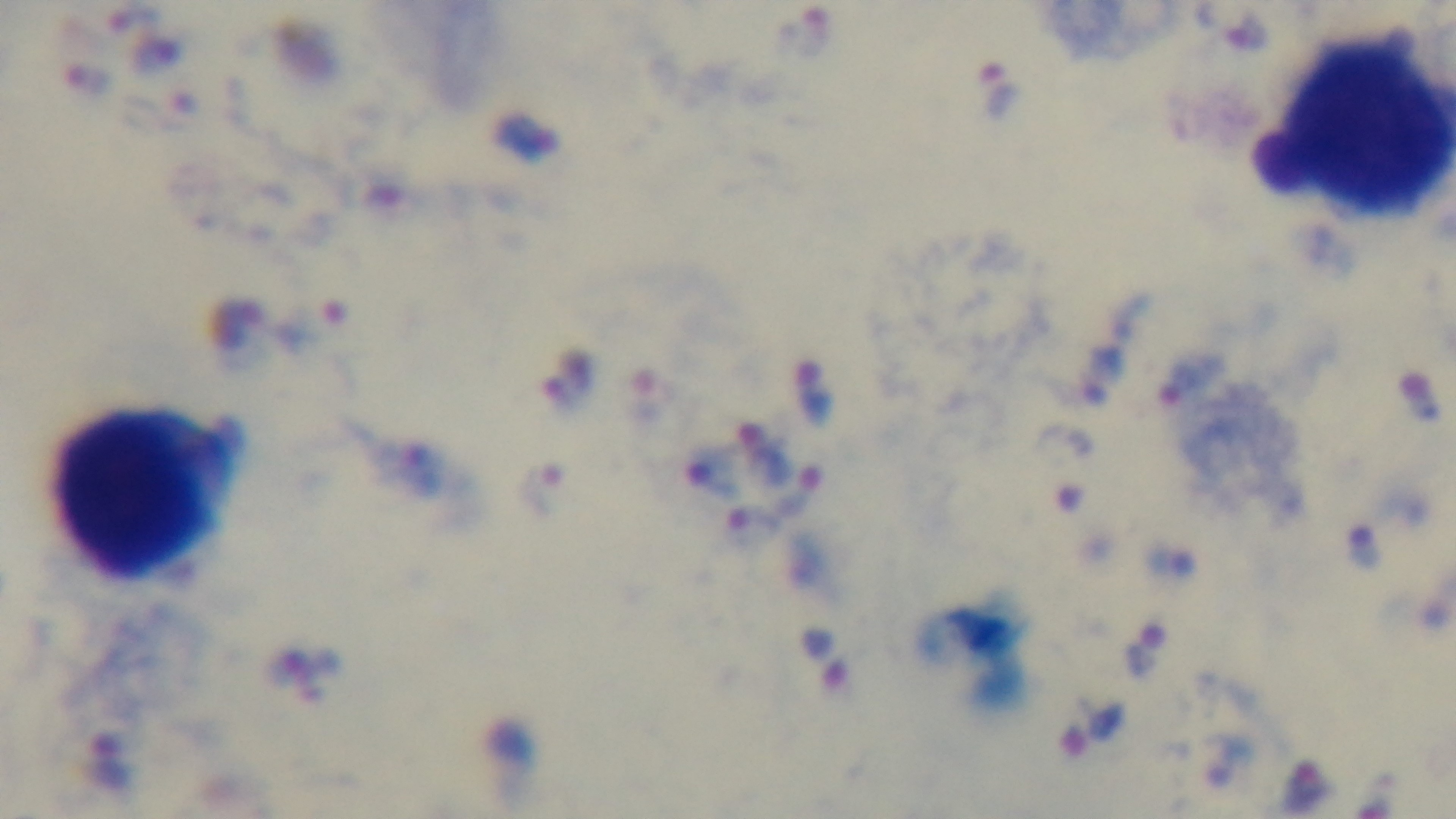
Summary:
  - Capture: mounted 4K digital camera
  - Malaria status: positive
  - Field of view: one from the slide
  - Preparation: thick smear
  - Modality: light microscopy
  - Stain: Giemsa
  - Objective: 100x oil immersion